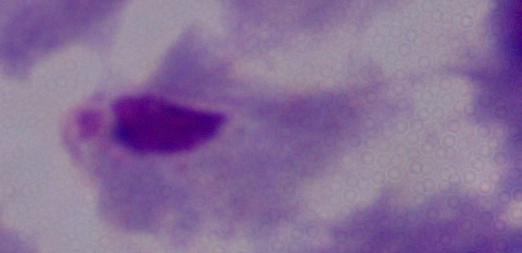
{
  "identification": "trichomonad",
  "magnification": "1000x",
  "modality": "micrograph"
}